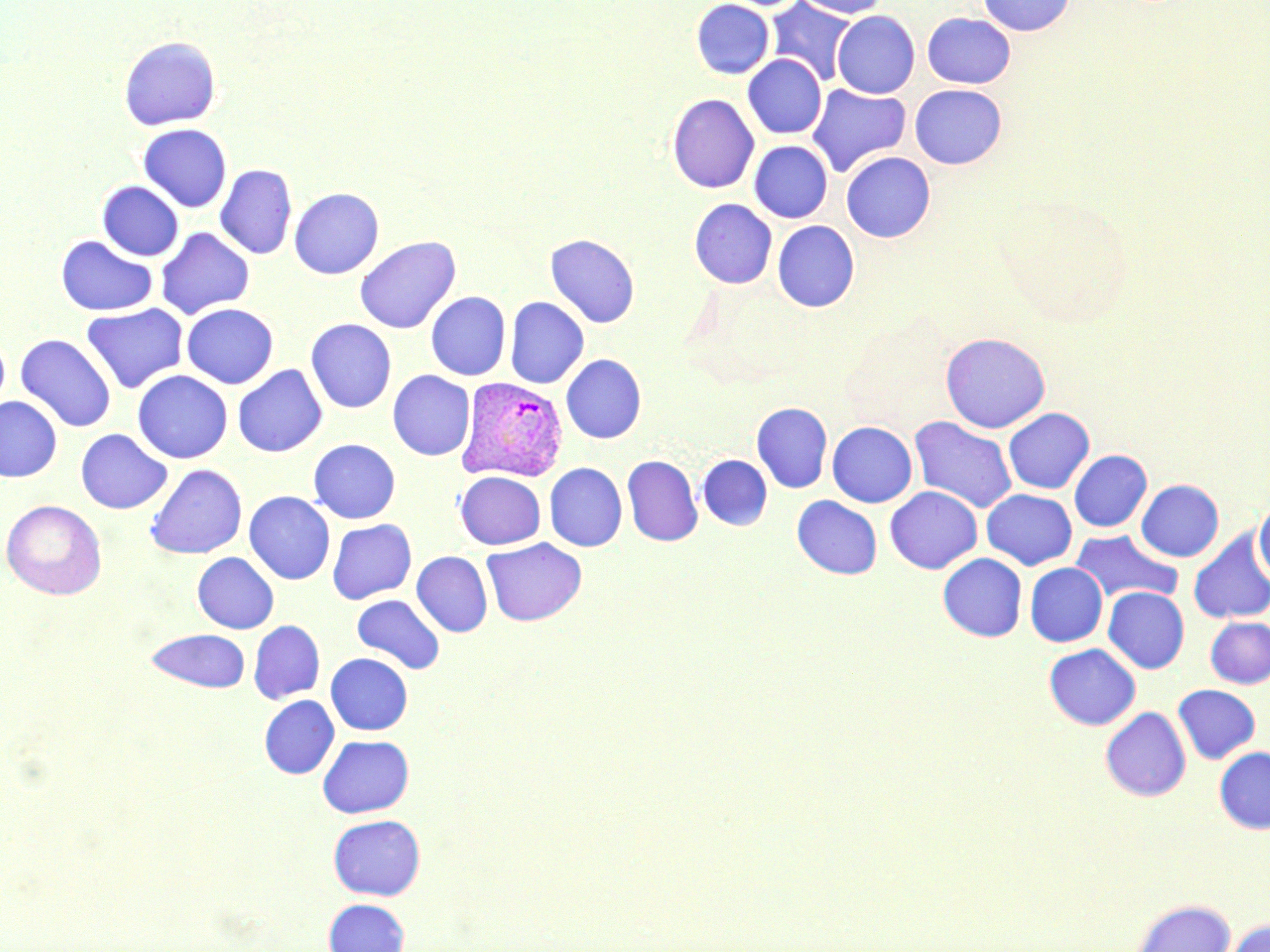 Approximate bounding boxes as (x1,y1)-(x2,y2) corner pairs in pixels. Uninfected red blood cell locations: (692,0)-(774,79), (765,0)-(857,85), (793,0)-(890,18), (978,0)-(1075,36), (833,10)-(920,98), (923,13)-(1016,88), (118,35)-(221,130), (743,54)-(827,138), (807,84)-(911,178), (909,84)-(1007,169), (667,93)-(759,193), (138,124)-(232,212), (749,141)-(832,222), (841,152)-(935,243), (215,164)-(298,260), (97,181)-(184,261), (289,187)-(384,279), (689,198)-(777,288), (772,221)-(859,312), (155,227)-(255,319), (56,234)-(158,316), (545,234)-(639,328), (355,236)-(461,334), (426,291)-(511,380), (505,297)-(589,389), (81,303)-(188,393), (181,303)-(278,389), (306,318)-(396,413), (0,332)-(10,416), (941,332)-(1050,433), (15,333)-(116,432), (561,354)-(646,443), (232,365)-(327,457), (133,370)-(232,463), (387,370)-(475,460), (0,396)-(62,482), (751,402)-(832,493), (1003,408)-(1094,494), (909,415)-(1018,514), (827,421)-(917,507), (76,428)-(172,514), (308,438)-(400,523), (1069,449)-(1152,532), (622,455)-(702,547), (697,455)-(772,530), (544,462)-(627,551), (145,463)-(247,559), (455,472)-(545,549), (1136,479)-(1224,561), (885,486)-(982,573), (982,489)-(1077,570), (244,491)-(335,584), (792,495)-(882,579), (2,500)-(107,600), (1255,501)-(1270,585), (327,519)-(416,604), (1188,528)-(1270,624), (1069,529)-(1183,605), (482,538)-(586,626), (412,551)-(493,637), (192,552)-(279,633), (938,553)-(1027,642), (1025,563)-(1108,647), (1103,587)-(1189,673), (352,594)-(445,674), (1205,617)-(1270,688), (249,620)-(325,704), (146,628)-(251,693), (1044,643)-(1140,730), (325,653)-(413,735), (1173,684)-(1260,764), (259,695)-(338,779), (1101,707)-(1191,801), (317,734)-(414,818), (1215,746)-(1270,833), (328,814)-(425,900), (323,898)-(410,952), (1132,898)-(1235,952), (1221,919)-(1270,952). Plasmodium vivax-infected red blood cell locations: (457,376)-(569,482). Slide-level diagnosis: Plasmodium vivax. One field of a larger specimen. Thin blood smear. May-Grünwald-Giemsa stain. Captured at 1000x magnification. Optical microscopy. Image is 1270×952 pixels.